Classify this cell by malaria status.
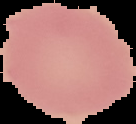

Uninfected.

Summary:
  - Preparation: thin blood film
  - Image type: segmented cell region with the area outside set to black
  - Image size: 136×124 pixels